Report the malaria status of this cell.
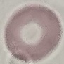
It is uninfected.

Summary:
  - Preparation: thin blood film
  - Stain: Giemsa
  - Capture: smartphone camera at the microscope eyepiece
  - Image type: cell patch, automatically extracted from a larger field of view and resized to 64 × 64 pixels